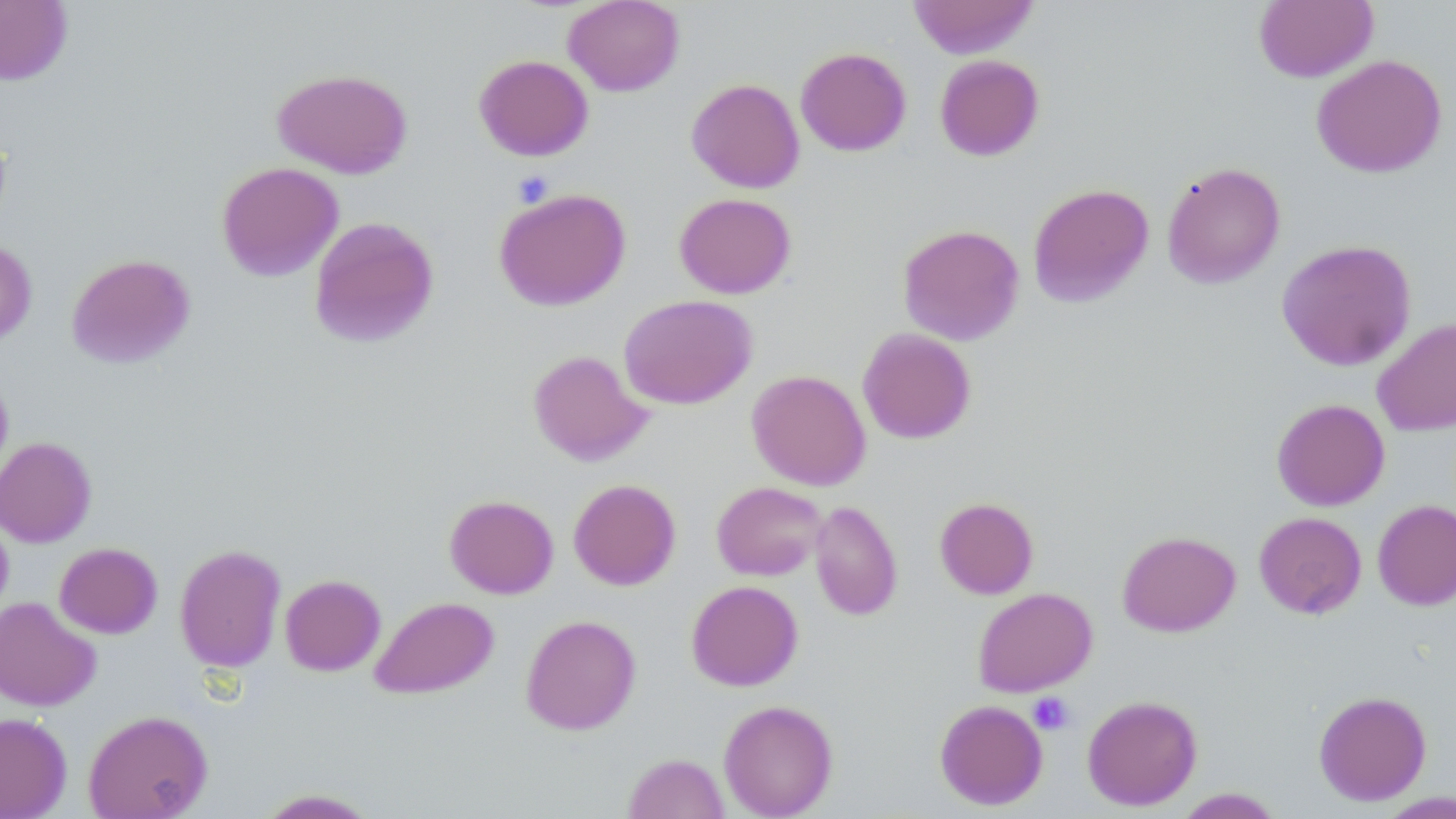

Approximate bounding boxes as (x1,y1)-(x2,y2) corner pairs in pixels. Platelet locations: (511,170)-(554,208), (1028,692)-(1075,735). Uninfected red blood cell locations: (0,0)-(72,86), (563,0)-(684,96), (907,0)-(1039,59), (1254,1)-(1378,82), (795,47)-(911,156), (474,54)-(594,160), (1311,54)-(1447,178), (935,55)-(1044,161), (272,68)-(413,178), (686,78)-(805,193), (216,161)-(343,281), (1162,161)-(1286,288), (1027,183)-(1154,308), (493,187)-(631,311), (674,192)-(796,298), (308,216)-(439,348), (897,223)-(1024,345), (1276,238)-(1417,371), (0,240)-(37,349), (65,253)-(195,369), (619,294)-(757,409), (1372,317)-(1456,436), (858,327)-(976,444), (528,349)-(654,466), (0,370)-(14,489), (746,370)-(871,490), (1271,398)-(1390,510), (0,436)-(97,547), (568,478)-(681,590), (711,481)-(827,581), (444,494)-(559,598), (935,497)-(1038,599), (1373,499)-(1456,610), (810,500)-(903,620), (0,511)-(14,621), (1254,512)-(1367,619), (1117,530)-(1241,636), (54,542)-(163,638), (174,543)-(286,673), (280,574)-(386,676), (686,580)-(803,691), (972,587)-(1097,696), (369,595)-(499,699), (0,597)-(101,710), (520,614)-(641,735), (1313,690)-(1432,805), (1082,694)-(1202,811), (934,699)-(1048,810), (718,700)-(838,818), (83,709)-(213,819), (0,712)-(72,819), (623,752)-(729,818), (254,788)-(381,818), (1173,788)-(1284,818), (1377,791)-(1456,817). Slide-level diagnosis: negative for blood parasites. Thin blood film. Single field of view. May-Grünwald-Giemsa-stained preparation. 1000x magnification. Image is 1456×819 pixels. Optical microscopy.